State the blood parasite species.
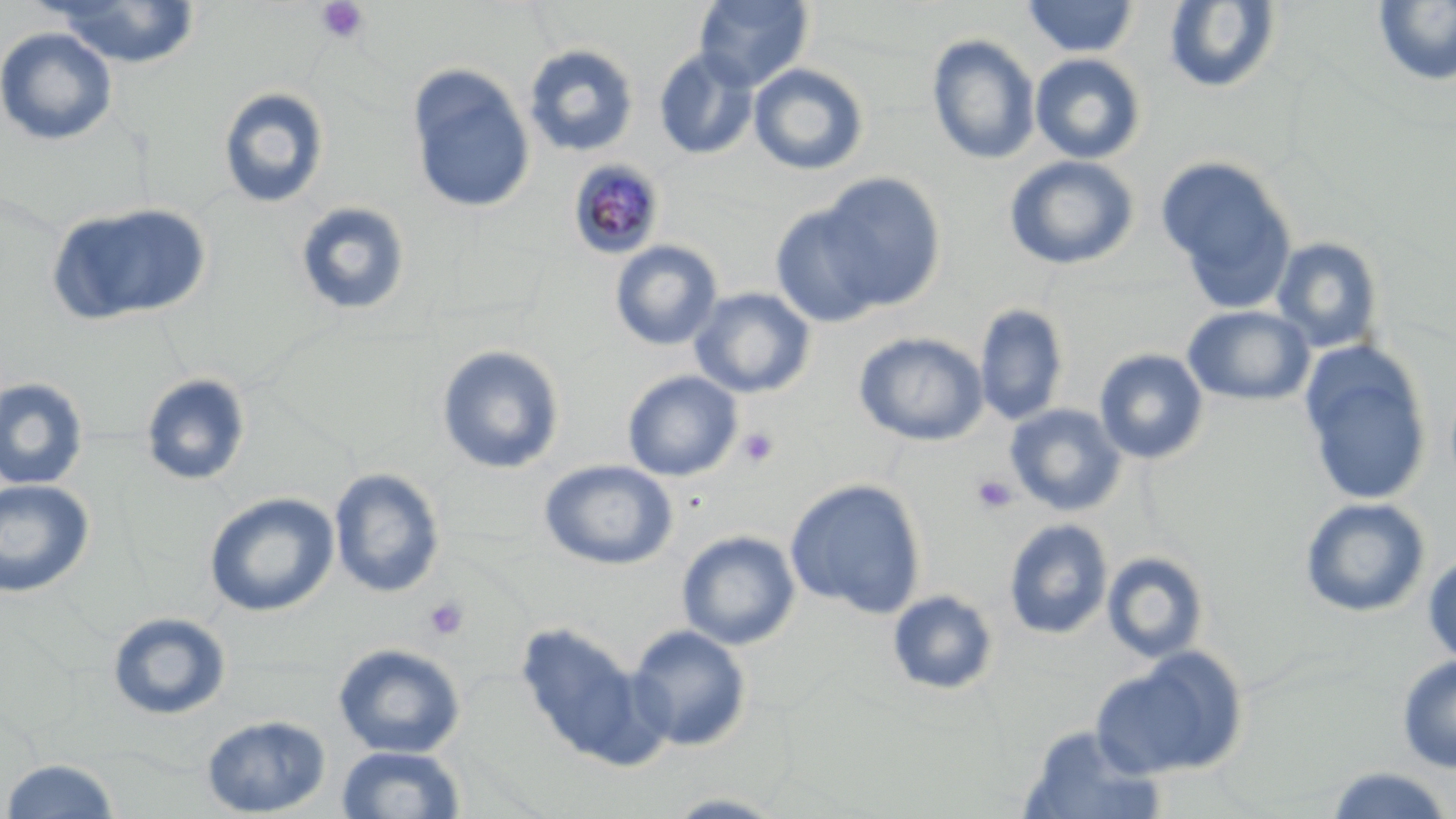
Plasmodium malariae.

Summary:
  - Coordinate format: approximate bounding boxes as named x1/y1/x2/y2 corners in pixels
  - Uninfected red blood cell locations: (x1=1020, y1=0, x2=1141, y2=59), (x1=44, y1=1, x2=203, y2=68), (x1=692, y1=1, x2=814, y2=91), (x1=1164, y1=1, x2=1282, y2=94), (x1=1372, y1=1, x2=1456, y2=87), (x1=0, y1=26, x2=118, y2=146), (x1=927, y1=34, x2=1041, y2=165), (x1=523, y1=44, x2=639, y2=157), (x1=654, y1=47, x2=758, y2=161), (x1=1029, y1=53, x2=1146, y2=164), (x1=749, y1=63, x2=869, y2=176), (x1=406, y1=64, x2=535, y2=215), (x1=218, y1=87, x2=330, y2=209), (x1=1004, y1=155, x2=1139, y2=270), (x1=1157, y1=155, x2=1298, y2=312), (x1=814, y1=173, x2=948, y2=312), (x1=294, y1=201, x2=412, y2=317), (x1=47, y1=202, x2=212, y2=326), (x1=770, y1=203, x2=888, y2=328), (x1=1271, y1=237, x2=1383, y2=354), (x1=609, y1=240, x2=723, y2=351), (x1=688, y1=287, x2=816, y2=399), (x1=975, y1=303, x2=1069, y2=426), (x1=1183, y1=305, x2=1315, y2=405), (x1=854, y1=331, x2=989, y2=446), (x1=1299, y1=341, x2=1433, y2=509), (x1=436, y1=344, x2=565, y2=475), (x1=1093, y1=348, x2=1209, y2=464), (x1=622, y1=370, x2=743, y2=481), (x1=140, y1=373, x2=251, y2=487), (x1=0, y1=377, x2=89, y2=490), (x1=1005, y1=403, x2=1127, y2=516), (x1=539, y1=459, x2=678, y2=570), (x1=329, y1=467, x2=445, y2=598), (x1=0, y1=478, x2=96, y2=598), (x1=785, y1=478, x2=928, y2=618), (x1=204, y1=492, x2=339, y2=618), (x1=1300, y1=497, x2=1431, y2=617), (x1=1003, y1=519, x2=1113, y2=639), (x1=677, y1=530, x2=801, y2=650), (x1=1422, y1=550, x2=1456, y2=668), (x1=1102, y1=552, x2=1209, y2=664), (x1=887, y1=589, x2=999, y2=696), (x1=107, y1=612, x2=232, y2=721), (x1=513, y1=621, x2=654, y2=767), (x1=627, y1=624, x2=752, y2=751), (x1=333, y1=642, x2=466, y2=758), (x1=1091, y1=648, x2=1247, y2=780), (x1=1396, y1=655, x2=1456, y2=773), (x1=201, y1=714, x2=331, y2=817), (x1=1019, y1=725, x2=1165, y2=819), (x1=337, y1=744, x2=466, y2=819), (x1=3, y1=759, x2=120, y2=817), (x1=1324, y1=766, x2=1455, y2=819), (x1=661, y1=791, x2=790, y2=818)
  - Platelet locations: (x1=316, y1=1, x2=369, y2=45), (x1=736, y1=426, x2=779, y2=468), (x1=971, y1=474, x2=1017, y2=514), (x1=423, y1=597, x2=470, y2=641)
  - Plasmodium malariae-infected red blood cell locations: (x1=567, y1=159, x2=666, y2=260)
  - Preparation: thin blood smear
  - Field of view: single
  - Stain: May-Grünwald-Giemsa
  - Image size: 1456×819 pixels
  - Magnification: 1000x
  - Modality: optical microscopy